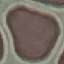
malaria status = uninfected
stain = Giemsa
preparation = thin smear
capture = smartphone camera at the microscope eyepiece
image type = cell patch, automatically extracted from a larger field of view and resized to 64 × 64 pixels